Comment on the morphology of the erythrocytes.
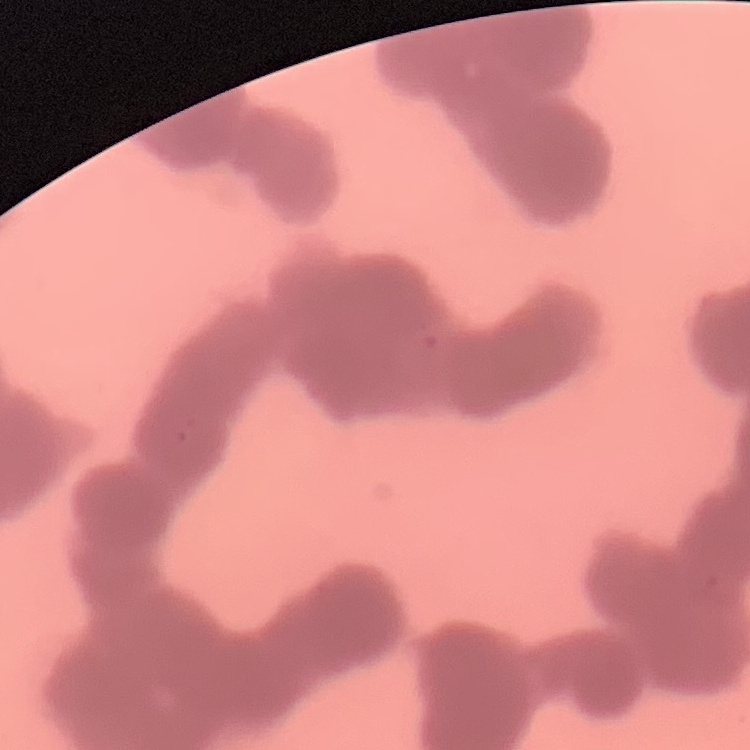
Rouleaux formation.

Summary:
  - Image type: square crop of a larger photomicrograph
  - Stain: Field's or Giemsa
  - Preparation: thin blood smear